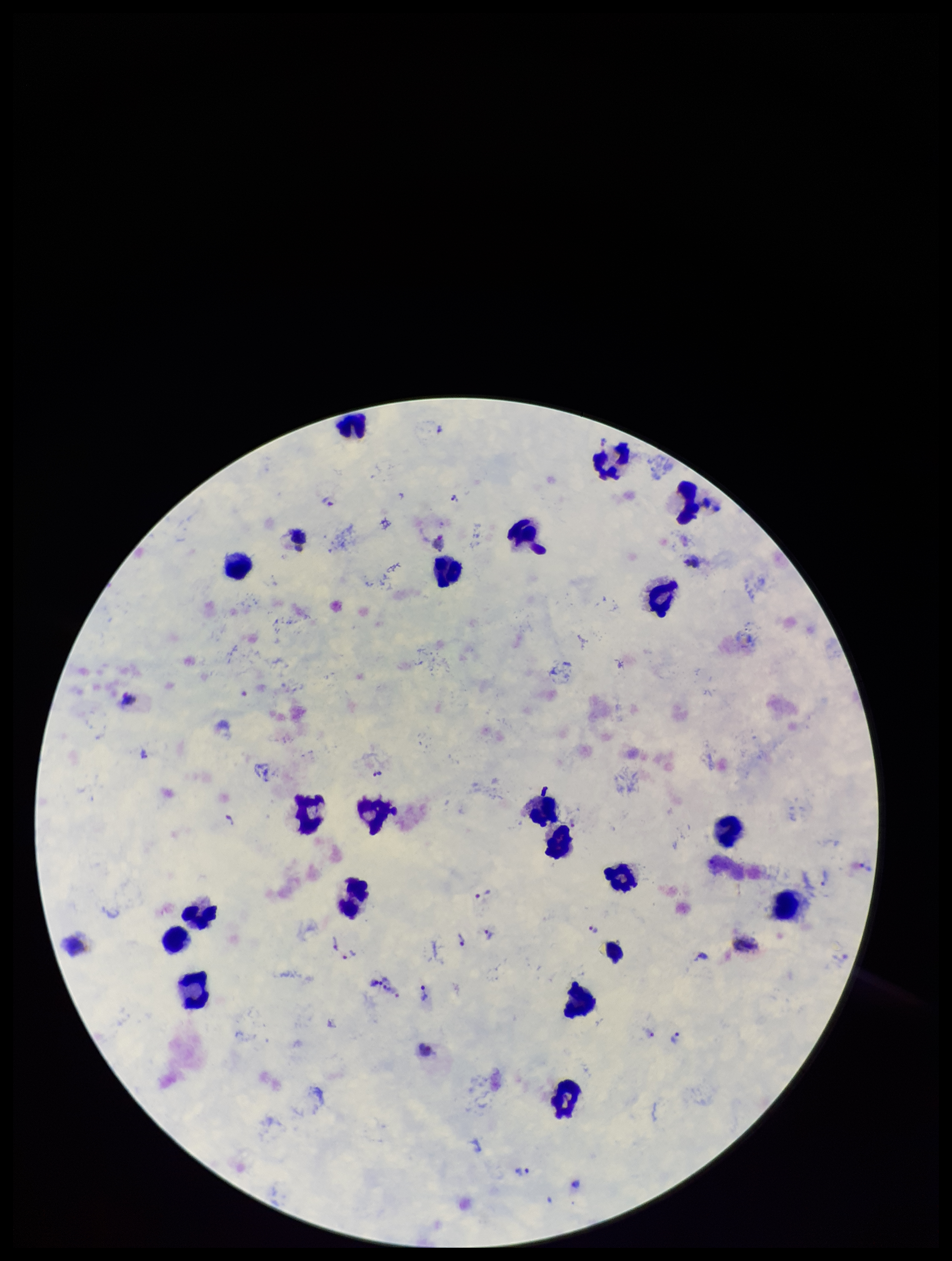
Summary:
  - Leukocyte count: 20
  - Parasite count: 19
  - Plasmodium parasites: identified
  - Field of view: one from this slide
  - Capture: smartphone photograph through the microscope eyepiece
  - Species reported for this patient: Plasmodium vivax
  - Patient malaria status: positive
  - Image size: 952×1261 pixels
  - Stain: Giemsa
  - Preparation: thick blood smear